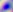
{
  "identification": "Toxoplasma gondii",
  "magnification": "400x",
  "modality": "photomicrograph"
}